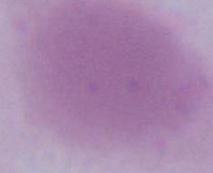
Summary:
  - Magnification: 1000x
  - Identification: erythrocyte
  - Modality: micrograph